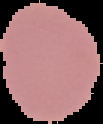

From a thin blood film. Result: no Plasmodium parasites detected. The area outside the segmented cell region is set to black. Image is 103×124 pixels.